Name the parasite shown.
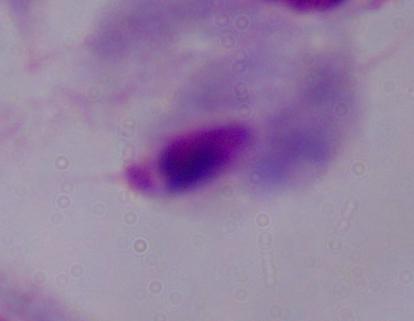

This is a trichomonad.

1000x magnification. Photomicrograph.